Locate every Plasmodium vivax-infected red blood cell.
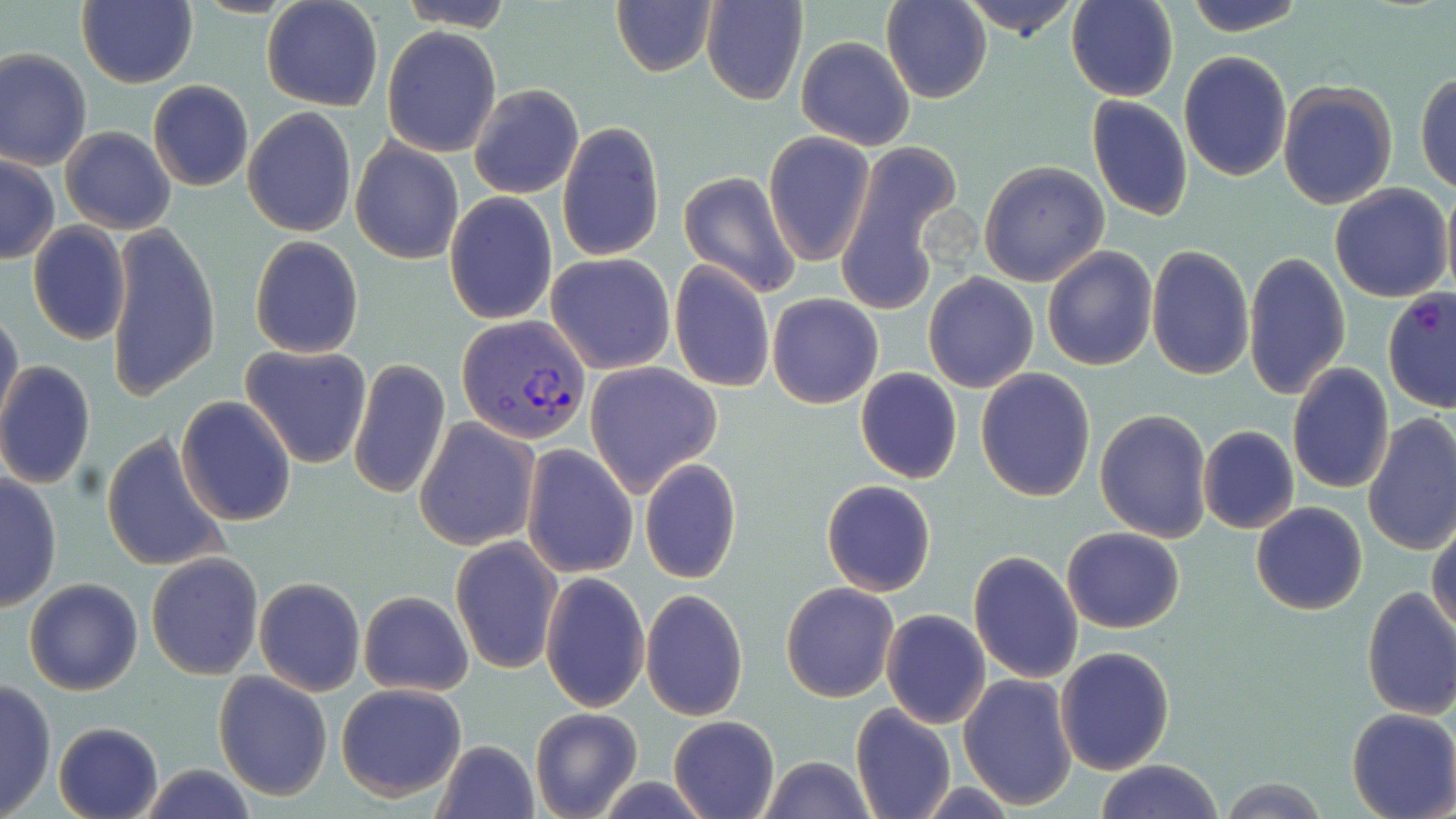

Approximate bounding boxes as (x1,y1)-(x2,y2) corner pairs in pixels.
Plasmodium vivax-infected red blood cells: (456,314)-(589,445).

Uninfected red blood cell locations: (77,0)-(198,89), (261,0)-(383,111), (395,0)-(514,30), (955,0)-(1084,43), (1066,0)-(1179,102), (1181,0)-(1307,37), (611,1)-(719,79), (701,1)-(807,105), (881,1)-(991,104), (382,26)-(501,158), (795,36)-(915,150), (1,48)-(93,171), (1178,51)-(1293,182), (1416,69)-(1456,196), (147,79)-(254,193), (1277,80)-(1398,210), (469,84)-(584,200), (1084,95)-(1192,223), (241,107)-(357,236), (557,120)-(664,264), (60,125)-(176,234), (763,132)-(876,266), (350,139)-(465,267), (836,143)-(961,317), (1,153)-(59,265), (979,160)-(1110,287), (677,170)-(802,299), (1329,183)-(1453,302), (1440,185)-(1456,305), (444,193)-(557,325), (26,222)-(130,347), (104,225)-(221,400), (249,237)-(363,359), (1146,242)-(1253,381), (1042,245)-(1157,371), (1244,251)-(1351,403), (546,253)-(676,374), (669,260)-(775,393), (923,271)-(1038,393), (1381,286)-(1456,415), (768,293)-(884,409), (0,306)-(23,434), (240,344)-(373,469), (348,358)-(451,501), (0,360)-(96,489), (585,363)-(722,496), (1287,363)-(1395,493), (855,367)-(963,484), (975,368)-(1095,502), (176,396)-(297,526), (1095,408)-(1213,543), (1361,413)-(1456,560), (414,418)-(538,550), (1197,425)-(1299,534), (101,431)-(233,574), (521,443)-(637,578), (639,459)-(741,584), (0,472)-(61,614), (822,479)-(936,596), (1250,501)-(1367,615), (1428,520)-(1456,638), (1061,526)-(1184,633), (450,536)-(563,675), (969,549)-(1084,685), (146,552)-(265,681), (540,572)-(650,713), (253,576)-(366,696), (23,577)-(143,695), (781,581)-(899,702), (1361,585)-(1456,720), (641,587)-(749,723), (358,590)-(474,696), (881,609)-(990,727), (1054,646)-(1176,776), (213,671)-(332,802), (957,674)-(1077,810), (0,677)-(57,818), (336,683)-(469,801), (849,703)-(955,819), (530,706)-(643,819), (1345,708)-(1456,819), (668,715)-(779,819), (51,721)-(164,819), (432,739)-(540,819), (759,755)-(875,819), (1093,758)-(1226,818), (132,763)-(262,819), (1217,778)-(1330,817). Slide-level diagnosis: Plasmodium vivax. Image is 1456×819 pixels. May-Grünwald-Giemsa stain. Light microscopy. Thin blood film. 1000x magnification. One field of a larger specimen.